Name the parasite shown.
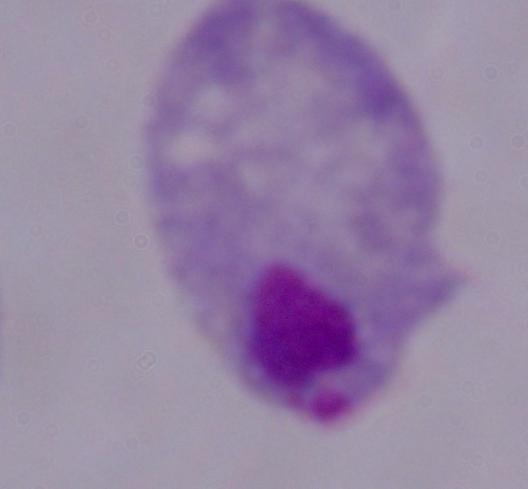

This is a trichomonad.

modality = micrograph
magnification = 1000x